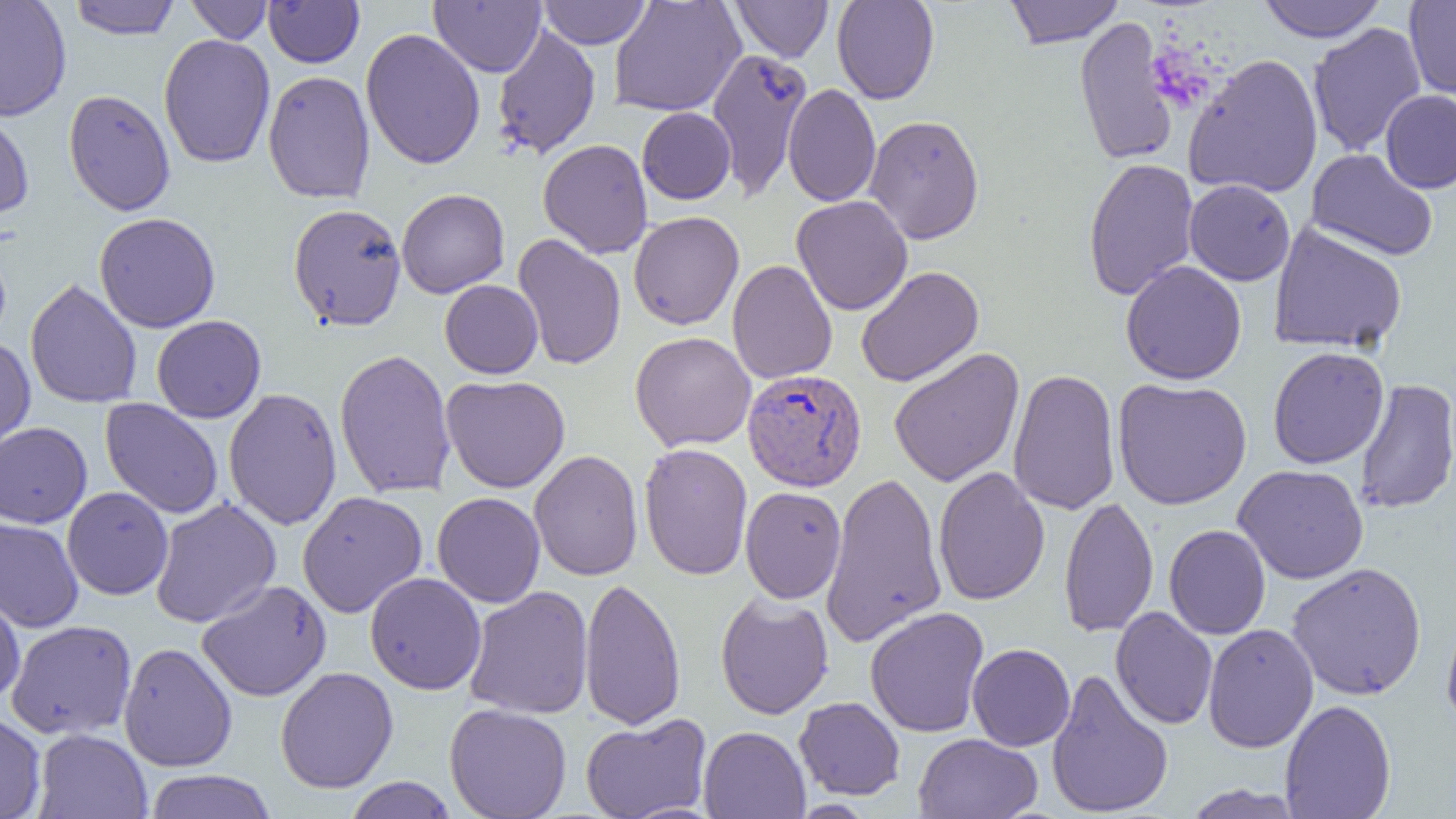
slide-level diagnosis = Plasmodium vivax
modality = light microscopy
field of view = single
preparation = thin blood smear
image size = 1456×819 pixels
Plasmodium vivax-infected red blood cell locations = approximate bounding boxes as (x1, y1, x2, y2) in pixels: (742, 368, 867, 492)
magnification = 1000x
uninfected red blood cell locations = approximate bounding boxes as (x1, y1, x2, y2) in pixels: (0, 0, 72, 121), (68, 0, 181, 39), (185, 0, 274, 43), (263, 0, 364, 68), (538, 0, 651, 49), (608, 0, 746, 117), (731, 0, 833, 62), (832, 0, 939, 104), (1003, 0, 1125, 49), (1256, 0, 1387, 43), (1403, 0, 1456, 100), (430, 1, 546, 76), (1074, 16, 1179, 167), (1307, 22, 1427, 157), (491, 24, 601, 160), (360, 28, 486, 170), (158, 34, 276, 168), (707, 48, 813, 201), (1184, 53, 1323, 199), (263, 70, 376, 204), (783, 84, 881, 207), (63, 88, 176, 216), (1380, 90, 1456, 193), (637, 107, 736, 205), (0, 110, 34, 220), (864, 114, 985, 244), (538, 139, 653, 259), (1307, 148, 1438, 261), (1083, 157, 1199, 301), (1184, 179, 1296, 286), (396, 188, 510, 298), (791, 196, 913, 316), (288, 203, 407, 330), (629, 211, 744, 330), (93, 212, 221, 333), (1268, 222, 1407, 354), (512, 233, 626, 371), (727, 259, 837, 384), (1120, 260, 1247, 385), (856, 266, 984, 387), (25, 279, 143, 409), (440, 280, 543, 378), (152, 315, 266, 422), (630, 331, 756, 452), (0, 336, 36, 457), (888, 347, 1025, 487), (1267, 347, 1389, 469), (334, 348, 457, 499), (1008, 368, 1121, 516), (441, 374, 570, 493), (1112, 377, 1252, 510), (1354, 378, 1456, 515), (223, 387, 342, 530), (100, 399, 223, 518), (0, 422, 92, 528), (638, 443, 753, 580), (529, 449, 643, 581), (1233, 464, 1369, 584), (933, 466, 1050, 606), (821, 471, 947, 648), (62, 486, 174, 600), (740, 486, 847, 604), (298, 491, 428, 617), (432, 492, 545, 608), (1059, 496, 1158, 638), (150, 498, 281, 628), (0, 516, 84, 632), (1164, 524, 1271, 640), (1286, 562, 1427, 701), (365, 572, 487, 695), (579, 577, 686, 731), (196, 580, 331, 702), (463, 586, 593, 719), (0, 590, 25, 703), (715, 591, 834, 719), (864, 606, 989, 737), (1110, 606, 1218, 729), (1441, 612, 1456, 733), (5, 620, 136, 740), (1203, 623, 1319, 753), (118, 642, 238, 772), (967, 643, 1075, 751), (275, 666, 398, 794), (1046, 668, 1174, 818), (794, 697, 906, 800), (1279, 699, 1396, 819), (444, 703, 572, 819), (0, 713, 46, 819), (580, 713, 711, 819), (698, 725, 810, 819), (33, 729, 152, 818), (913, 733, 1043, 819), (143, 769, 277, 819), (343, 777, 458, 818), (1180, 784, 1305, 818)